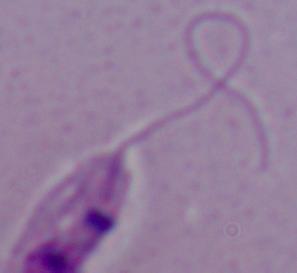
modality = micrograph
magnification = 1000x
identification = Leishmania